Identify the parasite.
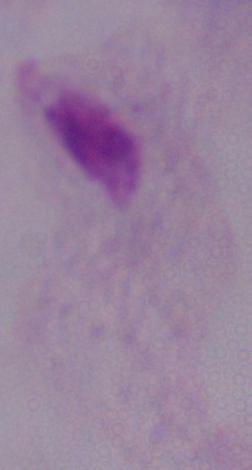

A trichomonad.

1000x magnification. Micrograph.